Locate malaria parasites and leukocytes.
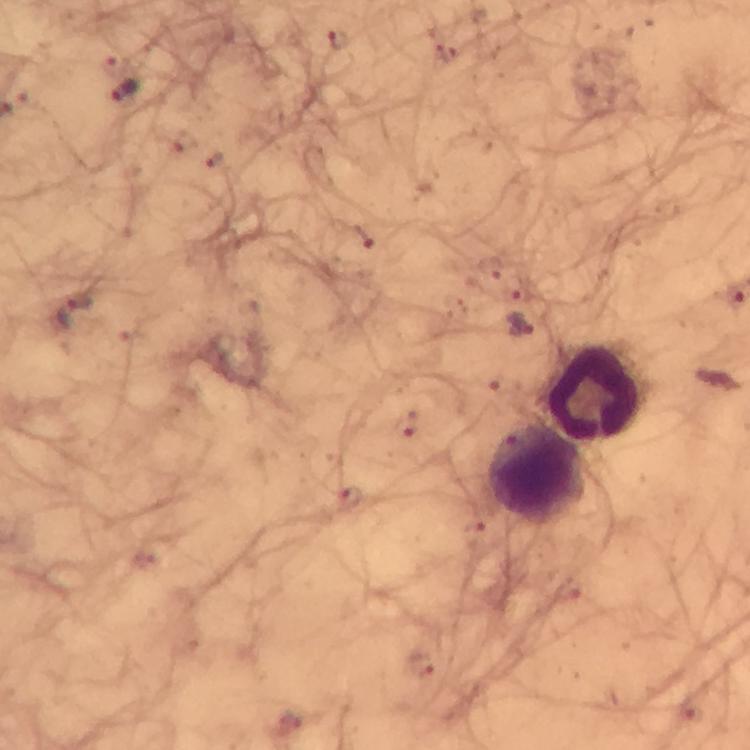

Approximate centers as (x, y) in pixels.
Malaria parasites: (339, 39), (125, 90), (214, 160), (364, 238), (519, 326), (405, 423), (350, 499).
Leukocytes: (594, 392), (537, 474).

Summary:
  - Stain: Giemsa
  - Magnification: 100x
  - Cropped from: a single field of view
  - Immersion oil: applied
  - Preparation: thick blood smear
  - Image size: 750×750 pixels
  - Context: from a diagnostic examination for malaria
  - Capture: smartphone mounted on the microscope